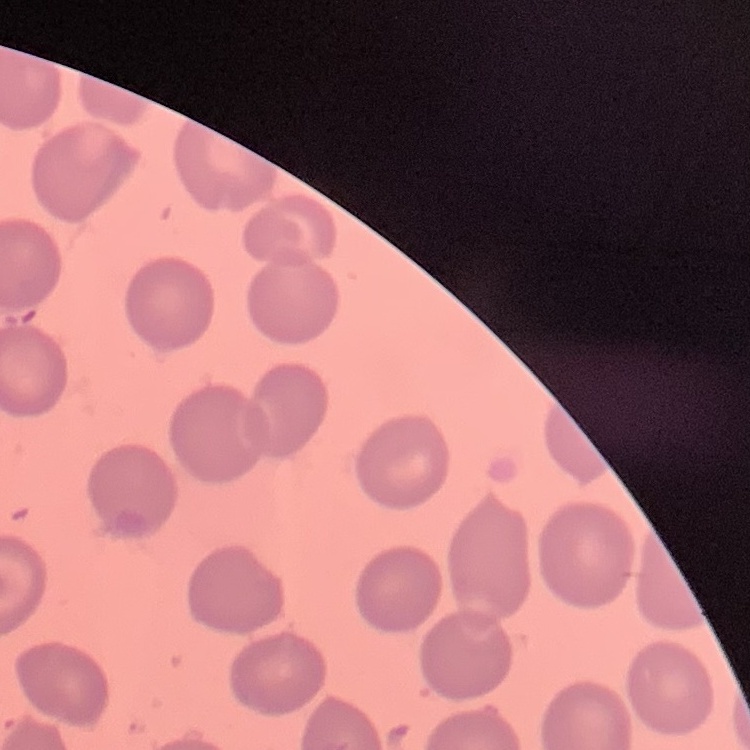
erythrocyte morphology = no rouleaux formation
image type = one tile cut from a larger photomicrograph
preparation = thin blood film
stain = Field's or Giemsa